Comment on the morphology of the erythrocytes.
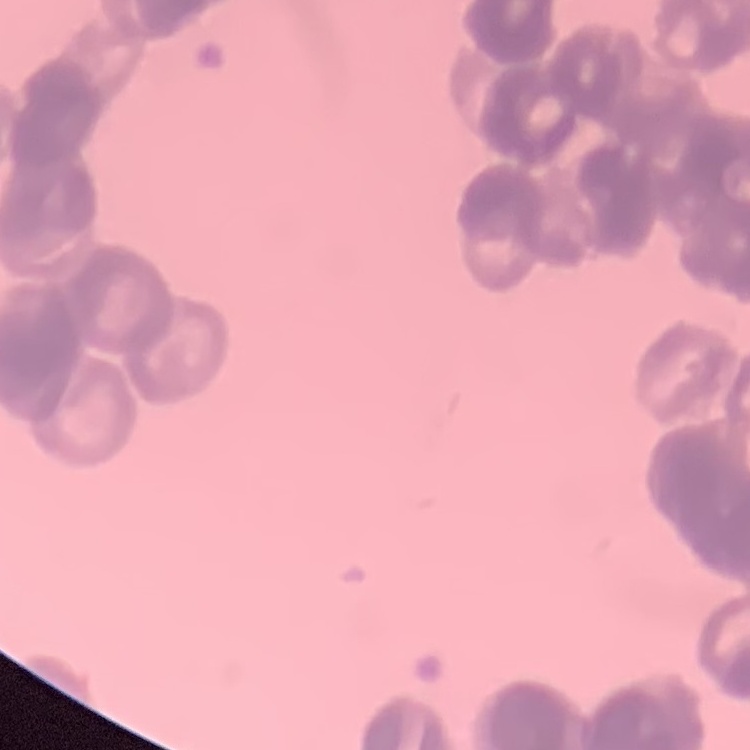

Rouleaux formation.

Summary:
  - Image type: one tile cut from a larger photomicrograph
  - Preparation: thin blood film
  - Stain: Field's or Giemsa